Name the parasite shown.
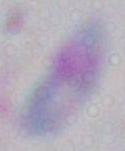
This is Toxoplasma gondii.

Summary:
  - Modality: photomicrograph
  - Magnification: 1000x